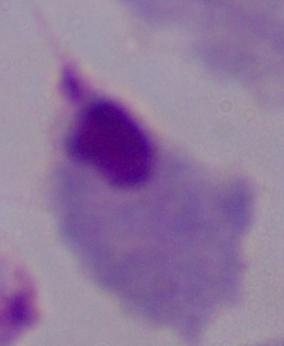 A trichomonad is seen. Photomicrograph. 1000x magnification.